Describe the morphology of the red blood cells.
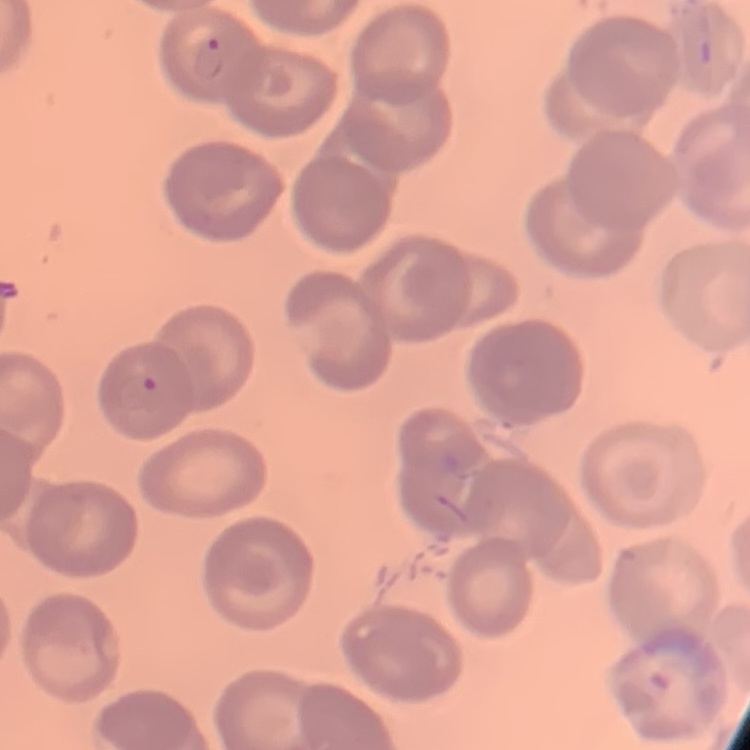

No rouleaux formation.

{
  "stain": "Field's or Giemsa",
  "preparation": "thin peripheral smear",
  "image_type": "square crop of a larger photomicrograph"
}